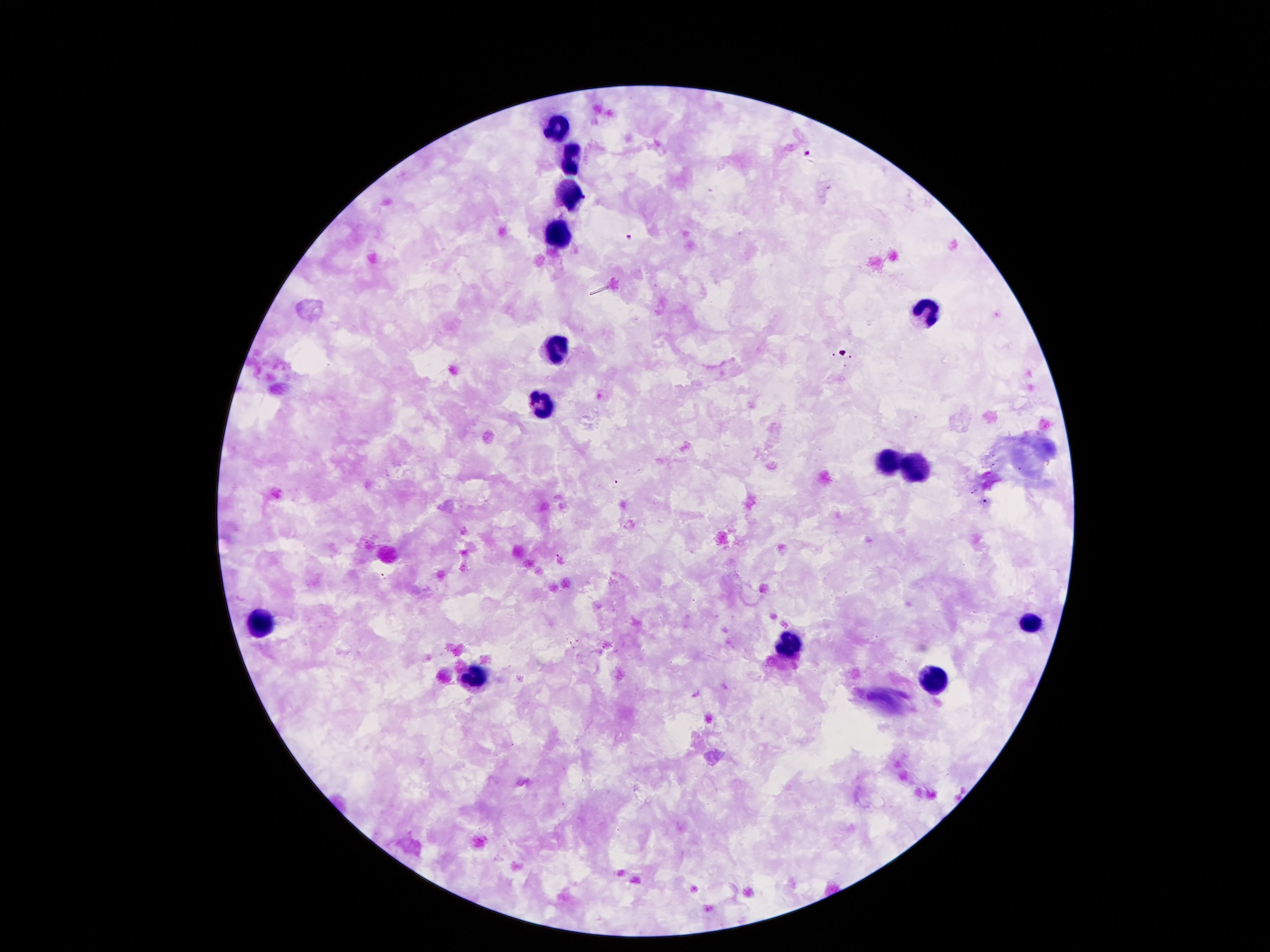

Approximate centers as (x, y) in pixels.
Summary:
  - Leukocyte locations: (558, 128), (569, 162), (567, 194), (558, 233), (928, 312), (558, 352), (541, 405), (889, 464), (912, 469), (1029, 622), (266, 624), (791, 643), (472, 676), (933, 680)
  - Malaria parasite locations: (806, 154), (630, 238)
  - Image size: 1270×952 pixels
  - Stain: Giemsa
  - Capture: smartphone through the microscope eyepiece
  - Field of view: single
  - Patient malaria status: positive for Plasmodium falciparum
  - Magnification: 100x
  - Preparation: thick peripheral-blood smear